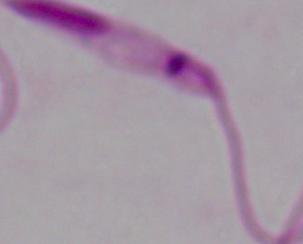
magnification: 1000x
identification: Leishmania
modality: photomicrograph